Assess this cell for malaria.
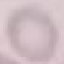
It is uninfected.

image_type: automatically extracted cell patch, resized to 64 × 64 pixels
capture: smartphone through the microscope eyepiece
stain: Giemsa
preparation: thin smear